Locate every blood parasite and identify its species.
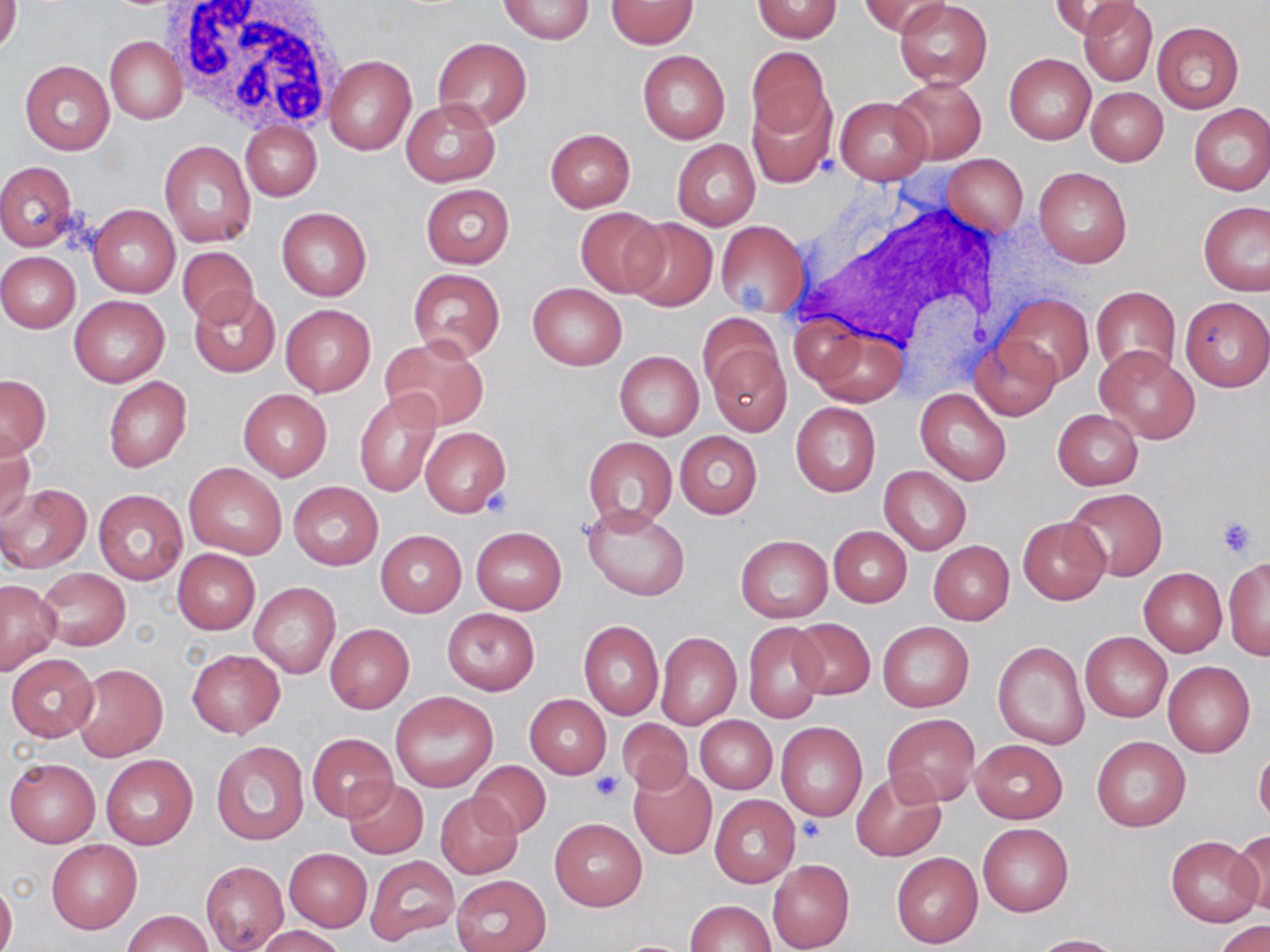

No blood parasites observed.

Summary:
  - Coordinate format: approximate bounding boxes as (x1,y1)-(x2,y2) corner pairs in pixels
  - Uninfected red blood cell locations: (0,0)-(21,56), (499,0)-(595,44), (861,0)-(949,37), (896,0)-(993,89), (1051,0)-(1140,40), (606,1)-(697,49), (752,1)-(842,42), (1078,2)-(1157,86), (1151,20)-(1244,114), (105,36)-(186,125), (432,37)-(532,129), (744,47)-(833,141), (637,50)-(730,143), (1004,53)-(1095,145), (324,54)-(417,156), (20,60)-(114,154), (891,77)-(987,165), (1086,87)-(1168,165), (746,92)-(835,188), (836,97)-(931,183), (400,99)-(500,186), (1188,103)-(1269,195), (241,122)-(321,201), (545,128)-(635,212), (160,140)-(255,248), (673,140)-(761,230), (943,154)-(1028,236), (0,162)-(78,252), (1034,168)-(1132,268), (420,184)-(515,268), (1199,201)-(1270,296), (89,205)-(180,298), (575,207)-(668,297), (276,208)-(371,302), (622,217)-(718,312), (715,220)-(810,318), (178,247)-(259,326), (0,251)-(81,332), (407,269)-(506,361), (527,282)-(627,371), (1091,286)-(1181,377), (189,287)-(280,379), (997,294)-(1092,387), (69,295)-(170,387), (1180,296)-(1270,390), (281,305)-(376,396), (697,314)-(781,399), (806,326)-(909,409), (381,335)-(489,430), (970,337)-(1060,420), (705,338)-(791,435), (1094,346)-(1199,444), (614,352)-(704,441), (1,375)-(51,458), (103,377)-(192,472), (238,389)-(332,480), (355,389)-(442,496), (915,389)-(1011,486), (790,401)-(881,497), (1052,409)-(1143,489), (419,427)-(511,517), (0,431)-(36,525), (675,431)-(762,518), (583,437)-(678,530), (184,462)-(286,559), (879,466)-(970,556), (288,482)-(382,569), (0,483)-(90,574), (1063,487)-(1167,581), (93,489)-(187,583), (583,503)-(690,602), (1018,517)-(1110,605), (827,526)-(911,607), (471,527)-(567,613), (375,530)-(466,617), (735,535)-(832,622), (928,541)-(1014,625), (173,549)-(260,633), (1224,558)-(1270,660), (1138,566)-(1227,657), (37,567)-(130,650), (0,580)-(60,674), (250,583)-(340,678), (443,608)-(540,694), (786,617)-(876,700), (579,620)-(663,720), (742,622)-(826,723), (325,623)-(414,712), (876,623)-(974,713), (1081,631)-(1172,723), (656,632)-(741,729), (992,639)-(1090,751), (187,649)-(284,738), (5,654)-(98,741), (1164,661)-(1255,757), (73,663)-(169,761), (390,692)-(497,791), (525,695)-(611,778), (882,714)-(980,806), (695,716)-(776,794), (616,719)-(694,795), (776,722)-(868,822), (307,734)-(396,821), (1091,735)-(1190,831), (971,740)-(1067,823), (211,741)-(309,844), (1254,745)-(1270,826), (100,753)-(198,850), (5,757)-(100,848), (468,760)-(551,838), (630,767)-(717,859), (852,772)-(946,861), (343,779)-(428,859), (435,792)-(522,879), (711,796)-(801,888), (550,818)-(647,910), (977,823)-(1074,917), (1230,830)-(1270,914), (1166,836)-(1263,926), (47,840)-(142,933), (285,848)-(371,931), (891,851)-(983,948), (366,854)-(458,945), (767,859)-(855,952), (200,860)-(288,952), (451,874)-(550,951), (0,878)-(17,952), (686,900)-(775,952), (123,910)-(212,952), (1215,920)-(1270,952), (254,925)-(347,952), (1030,934)-(1122,951)
  - White blood cell locations: (169,1)-(344,130), (787,189)-(1016,382)
  - Platelet locations: (483,489)-(514,516), (1215,514)-(1259,558), (591,772)-(623,802), (800,818)-(826,844)
  - Slide-level diagnosis: negative for blood parasites
  - Modality: optical microscopy
  - Field of view: one of a larger specimen
  - Preparation: thin blood smear
  - Stain: May-Grünwald-Giemsa
  - Magnification: 1000x
  - Image size: 1270×952 pixels